Outline each blood parasite and name the species.
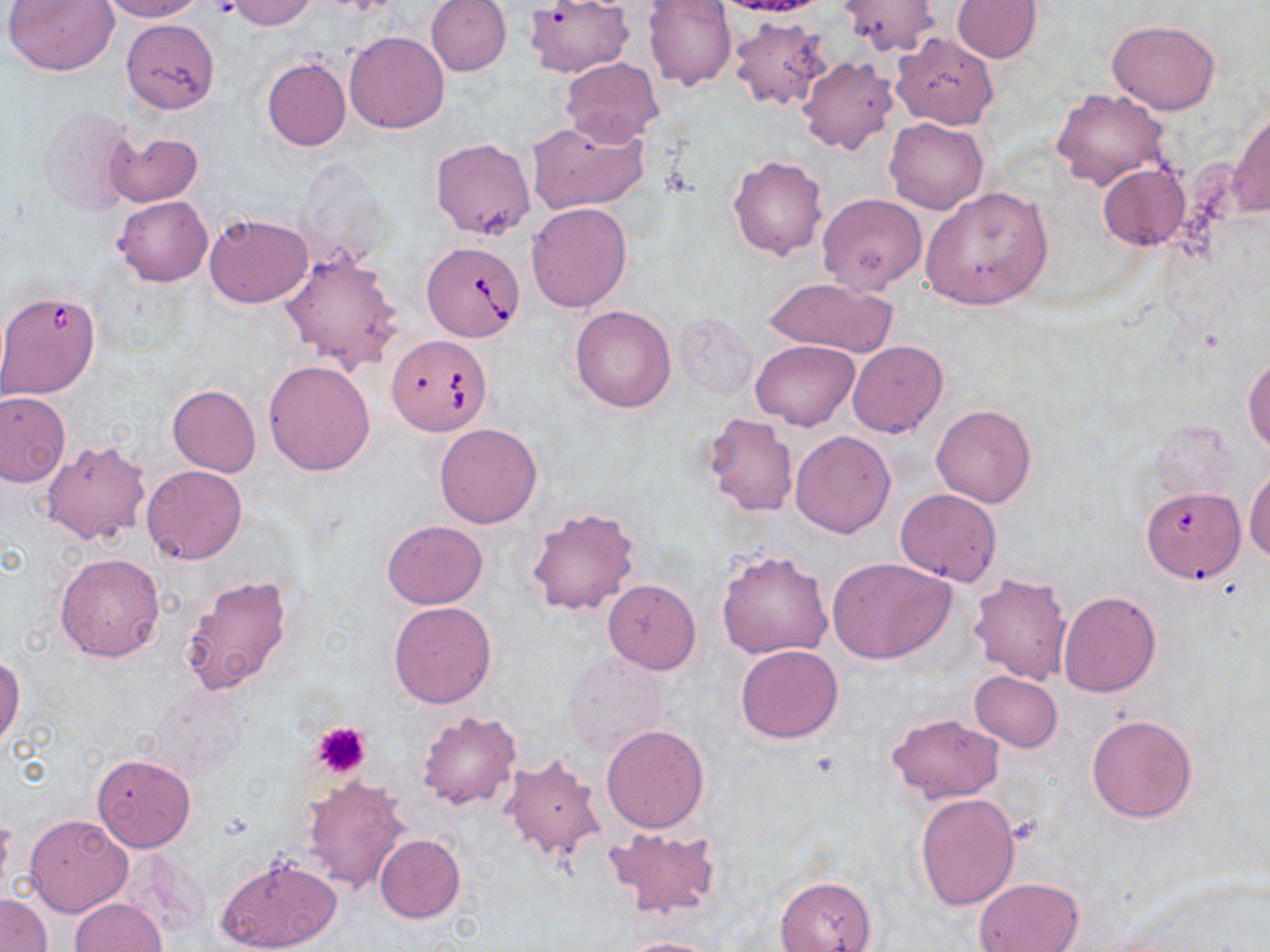

Approximate bounding boxes as (x1, y1, x2, y2) in pixels.
Babesia divergens-infected red blood cells: (425, 243, 528, 343), (0, 286, 102, 400), (389, 336, 490, 437).
No Plasmodium falciparum, Plasmodium ovale, Plasmodium malariae, Plasmodium vivax, or Trypanosoma brucei observed.

Platelet locations: (210, 1, 241, 21), (310, 721, 372, 778). Uninfected red blood cell locations: (5, 0, 116, 75), (101, 0, 205, 22), (227, 0, 318, 30), (425, 0, 512, 76), (524, 0, 632, 77), (643, 0, 737, 91), (713, 0, 832, 20), (836, 0, 943, 57), (951, 1, 1042, 62), (728, 16, 832, 110), (1107, 18, 1219, 115), (121, 19, 218, 113), (345, 30, 449, 133), (891, 32, 999, 130), (797, 55, 898, 154), (561, 56, 663, 143), (261, 57, 351, 152), (1053, 88, 1169, 191), (38, 105, 141, 218), (1230, 107, 1270, 219), (525, 117, 649, 216), (885, 117, 989, 214), (105, 130, 203, 207), (429, 138, 536, 239), (727, 155, 828, 261), (1097, 163, 1189, 251), (921, 186, 1053, 310), (817, 194, 927, 295), (113, 196, 213, 287), (526, 202, 632, 313), (204, 212, 313, 308), (277, 247, 406, 373), (762, 277, 898, 357), (569, 304, 677, 413), (676, 312, 757, 398), (752, 339, 858, 430), (847, 340, 948, 438), (1244, 356, 1270, 451), (263, 359, 377, 475), (168, 384, 260, 477), (0, 391, 70, 486), (931, 405, 1035, 508), (702, 413, 797, 517), (434, 423, 541, 527), (790, 430, 897, 537), (41, 440, 150, 546), (141, 464, 248, 565), (1245, 465, 1270, 565), (1141, 486, 1247, 594), (895, 488, 1001, 585), (525, 505, 639, 617), (382, 520, 487, 609), (716, 548, 832, 660), (55, 552, 166, 662), (827, 556, 958, 664), (967, 570, 1074, 686), (180, 574, 293, 696), (602, 580, 701, 673), (1057, 590, 1159, 697), (388, 600, 497, 708), (735, 645, 843, 743), (562, 652, 670, 759), (0, 653, 23, 749), (969, 669, 1062, 751), (416, 712, 521, 810), (884, 712, 1004, 803), (1087, 712, 1198, 822), (600, 723, 709, 833), (501, 737, 704, 848), (499, 751, 607, 864), (93, 754, 196, 853), (302, 774, 412, 893), (914, 792, 1020, 910), (0, 813, 14, 902), (25, 814, 133, 917), (603, 826, 722, 919), (374, 834, 466, 922), (117, 849, 206, 941), (215, 854, 343, 952), (775, 876, 877, 952), (973, 878, 1083, 952), (1, 892, 51, 952), (71, 898, 167, 952), (617, 937, 733, 952). Slide-level diagnosis: Babesia divergens. May-Grünwald-Giemsa-stained preparation. One field of a larger specimen. Image is 1270×952 pixels. Optical microscopy. Thin blood smear. 1000x magnification.